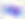

modality: micrograph
magnification: 400x
identification: Toxoplasma gondii